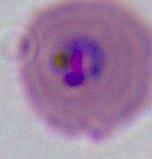

{
  "identification": "Plasmodium",
  "modality": "micrograph",
  "magnification": "400x or 1000x"
}